Describe the morphology of the erythrocytes.
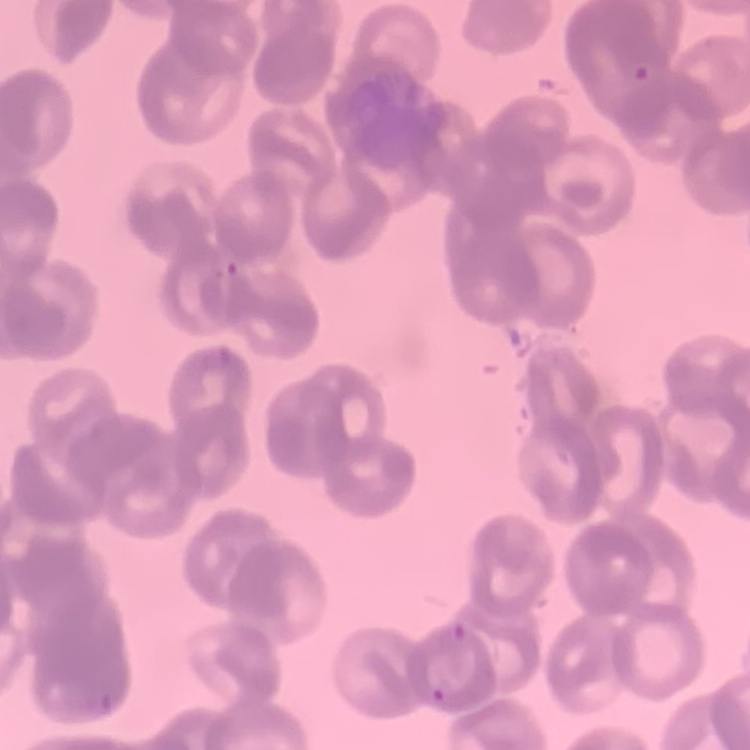
Rouleaux formation.

image type = square crop of a larger photomicrograph
stain = Field's or Giemsa
preparation = thin peripheral smear